Locate every uninfected red blood cell.
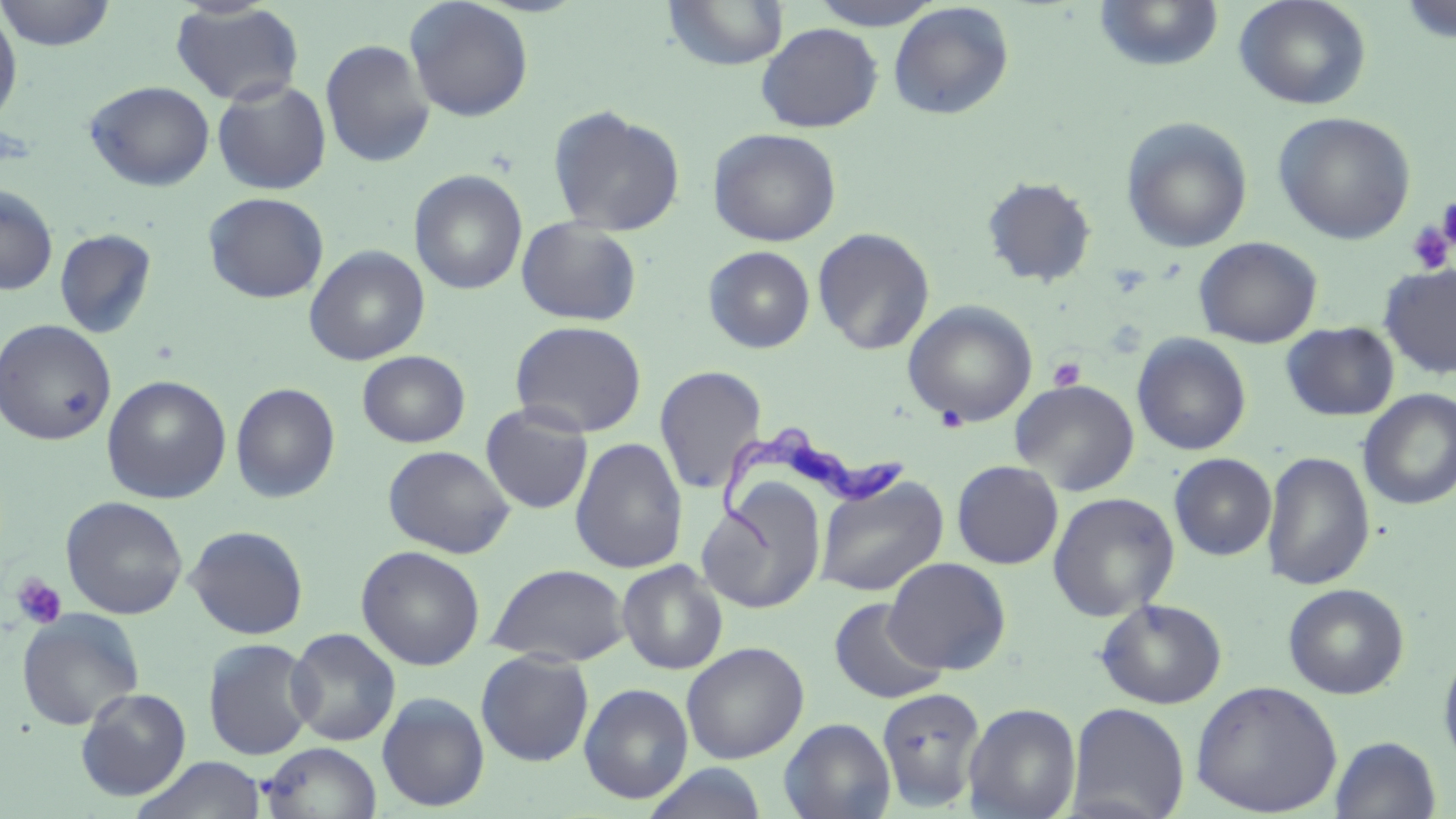

Approximate bounding boxes as [x1, y1, x2, y2] in pixels.
Uninfected red blood cells: [0, 0, 117, 51], [663, 0, 789, 70], [807, 0, 945, 30], [1092, 0, 1225, 72], [1234, 0, 1372, 110], [403, 1, 534, 122], [1399, 1, 1456, 44], [170, 2, 305, 106], [888, 2, 1014, 121], [0, 8, 23, 128], [756, 22, 883, 133], [319, 39, 435, 168], [211, 78, 332, 195], [84, 79, 215, 191], [547, 105, 686, 237], [1273, 111, 1416, 245], [1120, 116, 1254, 254], [708, 127, 842, 247], [409, 169, 527, 295], [981, 175, 1098, 288], [0, 184, 58, 295], [203, 192, 329, 303], [516, 217, 643, 327], [812, 227, 935, 355], [54, 228, 157, 338], [1193, 236, 1322, 348], [303, 245, 430, 365], [702, 245, 816, 354], [1378, 263, 1456, 379], [902, 300, 1038, 427], [0, 319, 117, 446], [509, 320, 647, 437], [1281, 322, 1399, 421], [1132, 333, 1251, 456], [357, 350, 470, 448], [654, 365, 767, 495], [101, 375, 232, 504], [1009, 378, 1140, 496], [229, 382, 341, 503], [1358, 390, 1456, 510], [479, 403, 594, 514], [570, 437, 688, 574], [382, 444, 516, 558], [1262, 451, 1376, 590], [1169, 453, 1276, 560], [951, 460, 1063, 569], [815, 475, 948, 597], [696, 484, 827, 615], [1047, 492, 1180, 621], [60, 496, 188, 620], [185, 524, 309, 639], [356, 545, 485, 671], [883, 556, 1011, 675], [617, 560, 728, 674], [487, 563, 631, 666], [1283, 582, 1409, 699], [827, 597, 948, 704], [1095, 598, 1228, 709], [16, 609, 145, 731], [286, 627, 401, 746], [202, 637, 318, 761], [681, 642, 809, 764], [1438, 643, 1456, 774], [475, 650, 594, 766], [1190, 680, 1343, 817], [579, 683, 693, 804], [876, 686, 986, 810], [76, 687, 192, 800], [377, 691, 490, 812], [964, 702, 1082, 819], [1066, 702, 1190, 819], [779, 717, 896, 819], [1329, 735, 1442, 819], [261, 742, 382, 819], [132, 756, 268, 818], [641, 763, 770, 819].

Platelet locations: [1437, 195, 1456, 254], [1406, 220, 1453, 274], [1048, 357, 1086, 392], [936, 406, 969, 433], [12, 574, 67, 629]. Trypanosoma brucei locations: [718, 421, 905, 552]. Slide-level diagnosis: Trypanosoma brucei. Thin blood smear. Image is 1456×819 pixels. One field of a larger specimen. May-Grünwald-Giemsa-stained preparation. Captured at 1000x magnification. Light microscopy.